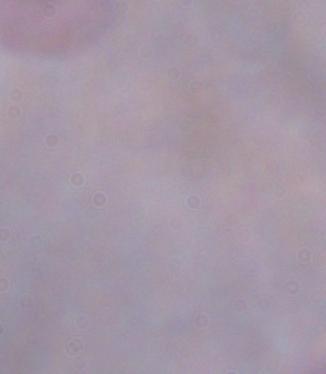

Summary:
  - Modality: photomicrograph
  - Identification: trypanosome
  - Magnification: 1000x